Describe the morphology of the erythrocytes.
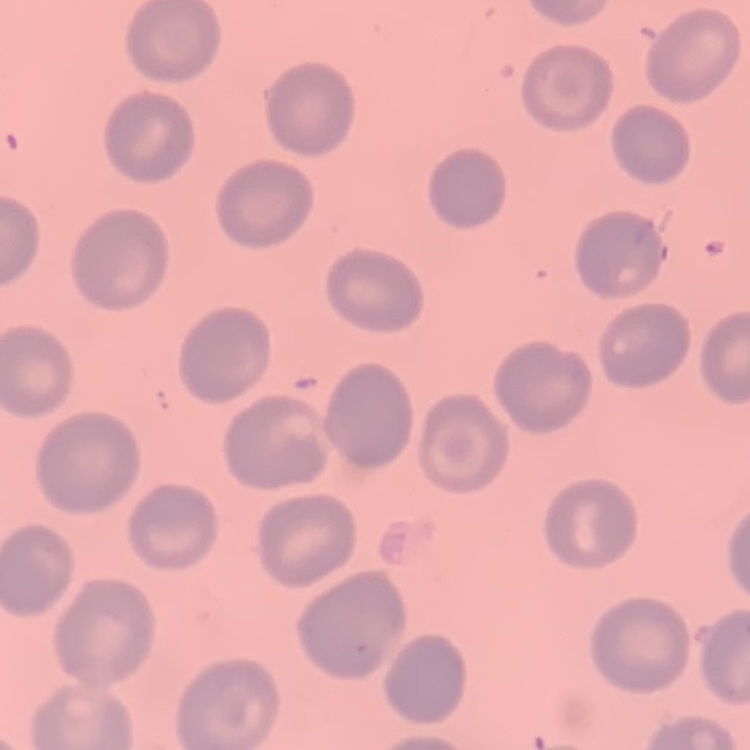
They show no rouleaux formation.

Thin blood smear. Square crop of a larger photomicrograph. Stained with either Field's or Giemsa.